Name the blood parasite species.
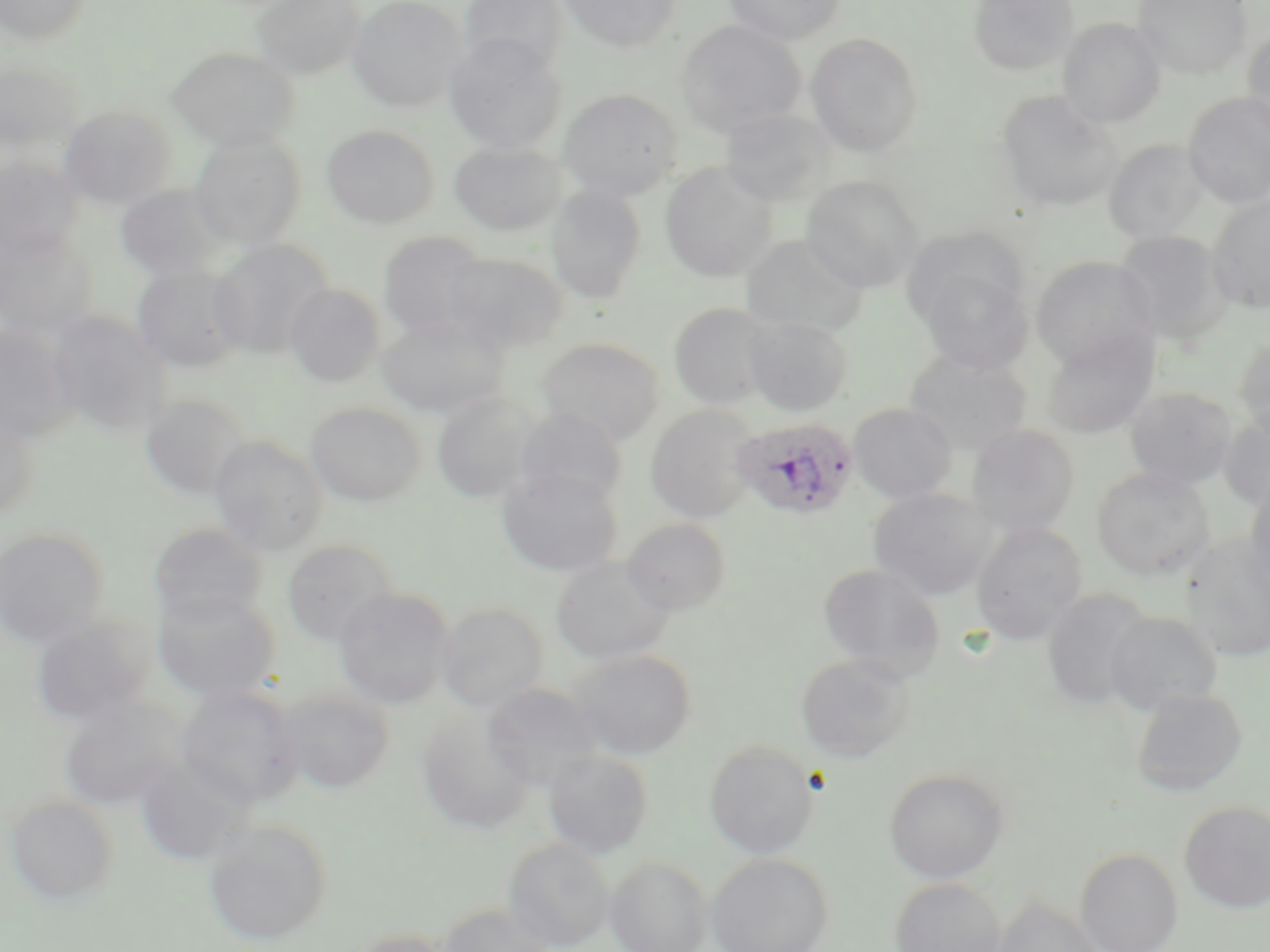
Plasmodium ovale.

stain = May-Grünwald-Giemsa
image size = 1270×952 pixels
uninfected red blood cell locations = approximate bounding boxes as (x1,y1)-(x2,y2) corner pairs in pixels: (1,0)-(92,45), (250,0)-(365,80), (348,0)-(464,111), (459,0)-(567,75), (560,0)-(681,51), (723,0)-(847,46), (968,0)-(1080,78), (1131,0)-(1251,78), (1058,18)-(1167,127), (676,20)-(805,136), (1242,24)-(1270,140), (806,32)-(924,156), (444,34)-(566,155), (167,47)-(299,150), (0,61)-(83,160), (558,89)-(683,202), (996,91)-(1120,212), (1183,91)-(1270,208), (57,105)-(176,210), (719,109)-(836,208), (322,125)-(439,228), (189,131)-(307,250), (1105,139)-(1213,246), (449,141)-(565,236), (0,157)-(83,264), (660,161)-(779,282), (801,175)-(924,292), (114,184)-(229,282), (546,185)-(647,305), (1207,195)-(1270,314), (902,227)-(1029,334), (378,231)-(495,343), (1115,231)-(1231,345), (0,232)-(98,343), (740,234)-(869,338), (208,240)-(334,359), (441,251)-(567,353), (1031,255)-(1158,370), (915,261)-(1033,374), (131,265)-(246,372), (285,283)-(385,389), (669,302)-(777,411), (45,311)-(169,437), (376,315)-(505,418), (744,315)-(853,416), (0,324)-(76,446), (1041,330)-(1158,439), (538,337)-(663,445), (1235,337)-(1270,441), (904,348)-(1032,456), (1125,387)-(1237,491), (431,392)-(542,504), (140,394)-(250,501), (305,402)-(425,507), (849,403)-(958,505), (645,404)-(762,523), (513,408)-(627,510), (1220,408)-(1270,515), (0,413)-(38,520), (966,423)-(1080,537), (209,436)-(328,556), (497,467)-(623,577), (1092,467)-(1215,581), (1243,480)-(1270,599), (869,488)-(999,602), (623,517)-(732,615), (971,522)-(1087,645), (148,523)-(267,624), (0,526)-(110,648), (1180,533)-(1270,662), (281,539)-(400,648), (551,557)-(674,665), (817,562)-(945,681), (152,588)-(281,705), (335,588)-(454,709), (1041,589)-(1155,711), (436,601)-(548,713), (1105,610)-(1222,714), (29,617)-(153,728), (566,648)-(696,760), (795,653)-(913,762), (273,682)-(395,795), (484,683)-(602,790), (176,686)-(304,809), (1130,688)-(1248,796), (58,698)-(186,811), (417,709)-(535,834), (704,739)-(820,859), (543,749)-(654,859), (132,757)-(248,867), (884,767)-(1009,883), (4,795)-(119,907), (1179,800)-(1270,914), (202,818)-(332,946), (504,838)-(613,952), (1075,847)-(1184,952), (705,853)-(834,952), (605,855)-(712,952), (889,878)-(1007,952), (991,897)-(1104,952), (437,903)-(557,952), (343,928)-(457,952)
modality = light microscopy
field of view = single
Plasmodium ovale-infected red blood cell locations = approximate bounding boxes as (x1,y1)-(x2,y2) corner pairs in pixels: (731,416)-(859,522)
preparation = thin blood film
magnification = 1000x